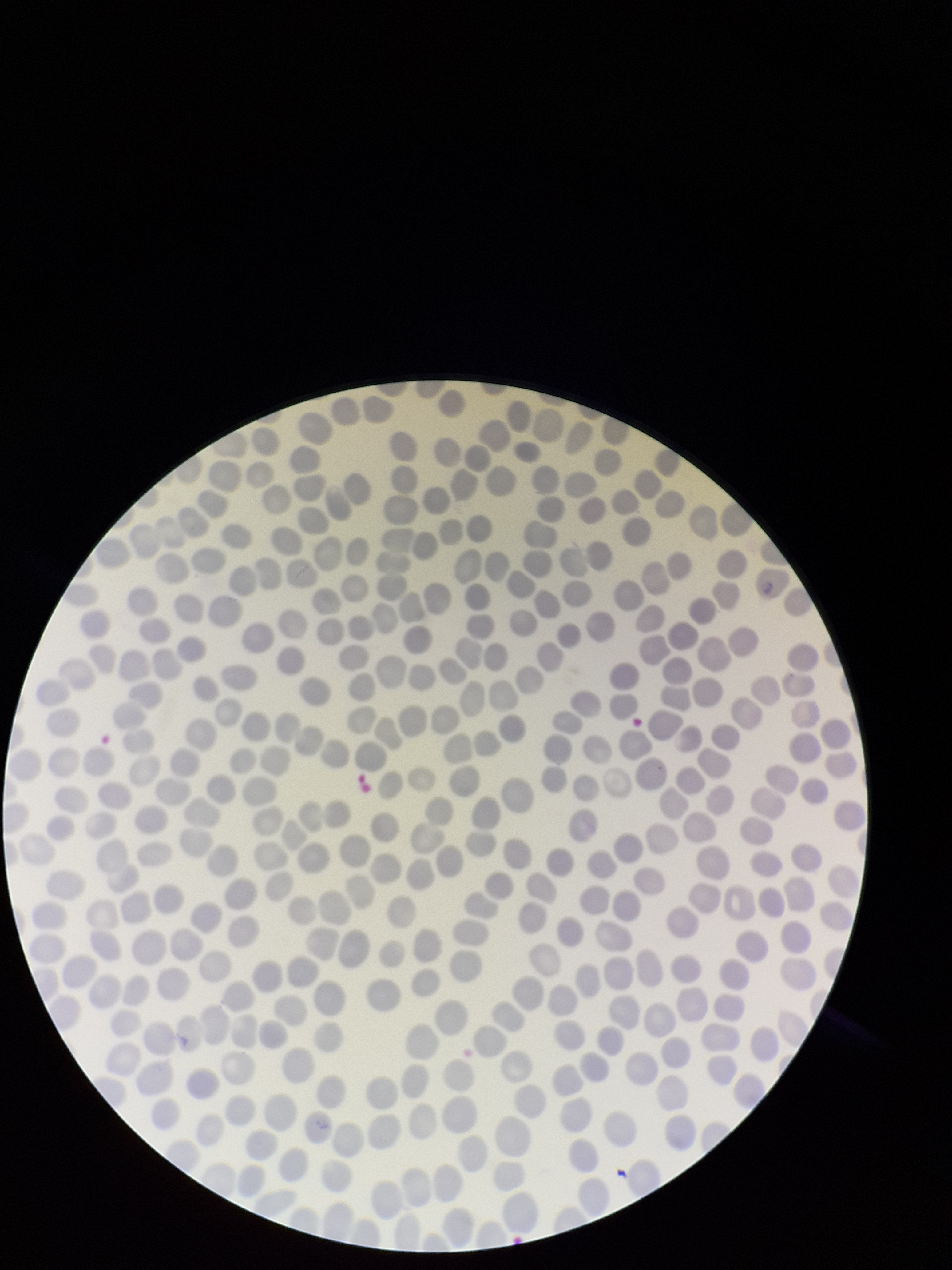
Summary:
  - Species reported for this patient: Plasmodium falciparum
  - Red blood cell count: 278
  - Stain: Giemsa
  - Patient malaria status: positive
  - Parasitized red blood cell count: 0
  - Parasitized red blood cells: none seen
  - Capture: smartphone photograph through the microscope eyepiece
  - Field of view: single
  - Image size: 952×1270 pixels
  - Preparation: thin smear